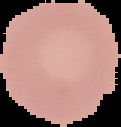
{
  "image_size": "121×127 pixels",
  "image_type": "cell region segmented out of the field of view; surrounding area masked to black",
  "result": "negative for malaria parasites",
  "preparation": "thin blood film"
}